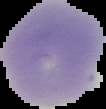
image type = segmented cell region with the area outside set to black
preparation = thin blood film
image size = 106×109 pixels
malaria status = uninfected